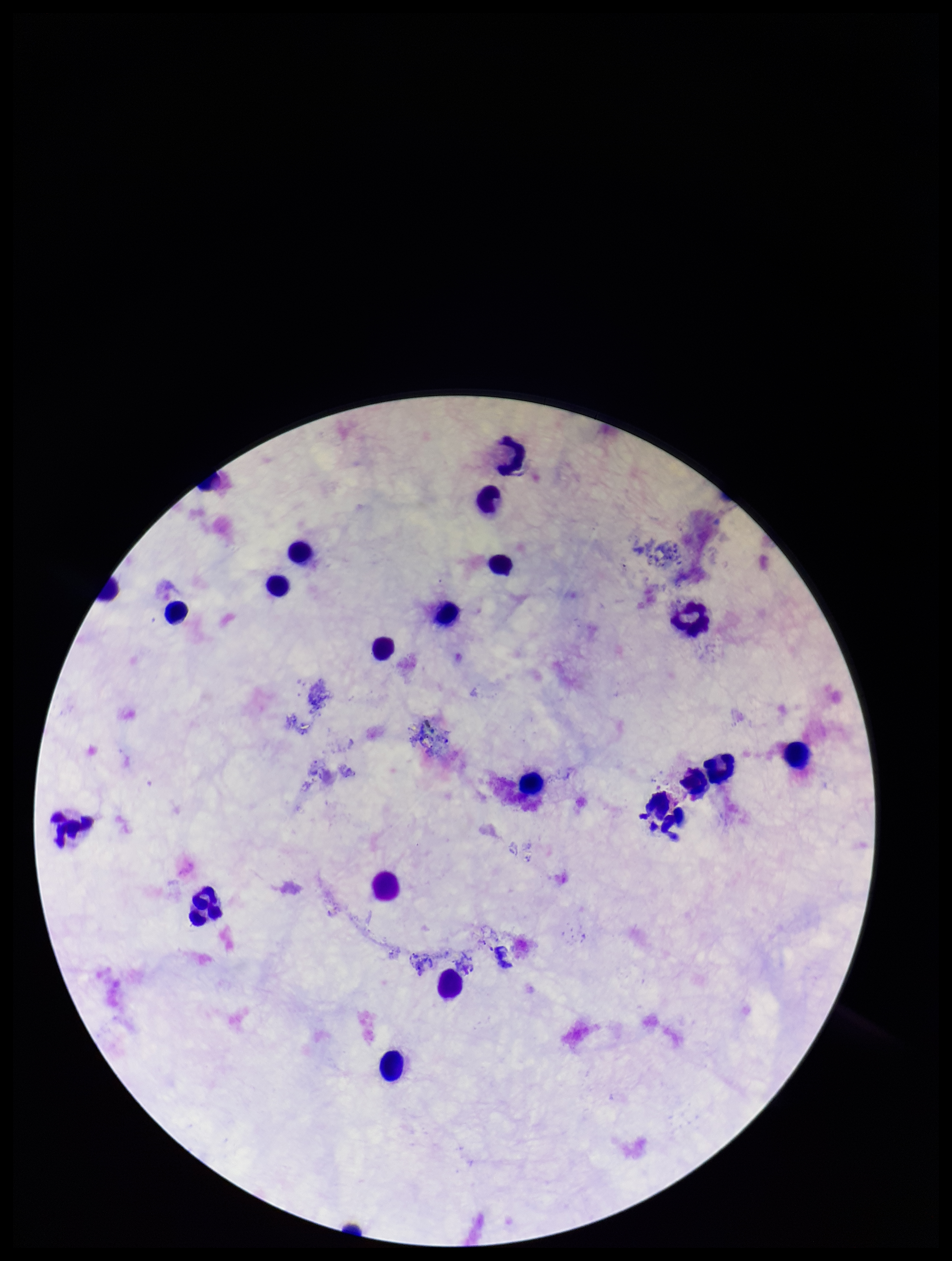
Plasmodium parasites = none identified
field of view = one from this slide
preparation = thick blood smear
stain = Giemsa
parasite count = 0
image size = 952×1261 pixels
capture = smartphone photograph through the microscope eyepiece
leukocyte count = 20
patient malaria status = negative